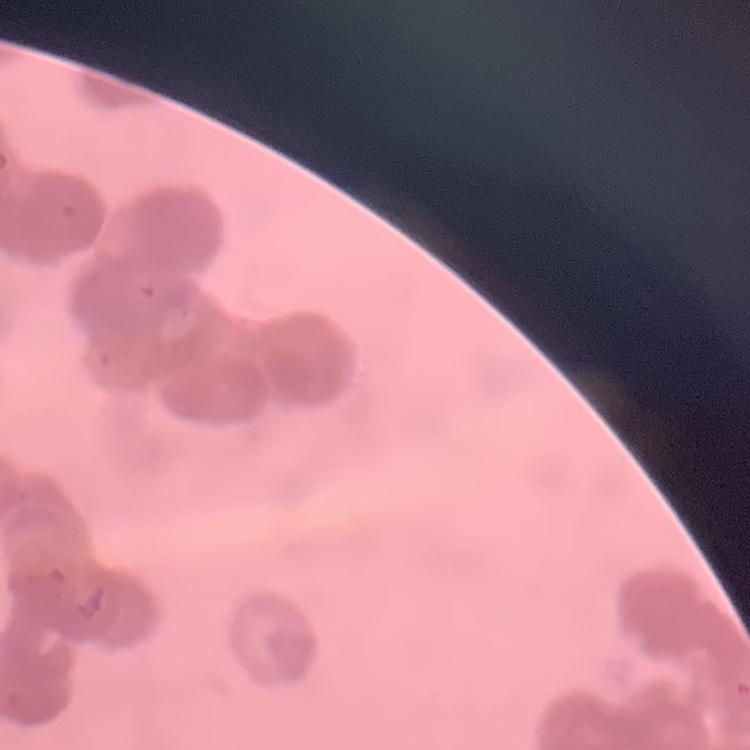

Summary:
  - Erythrocyte morphology: rouleaux formation
  - Image type: one tile cut from a larger photomicrograph
  - Stain: Field's or Giemsa
  - Preparation: thin peripheral smear